Locate and identify every blood parasite.
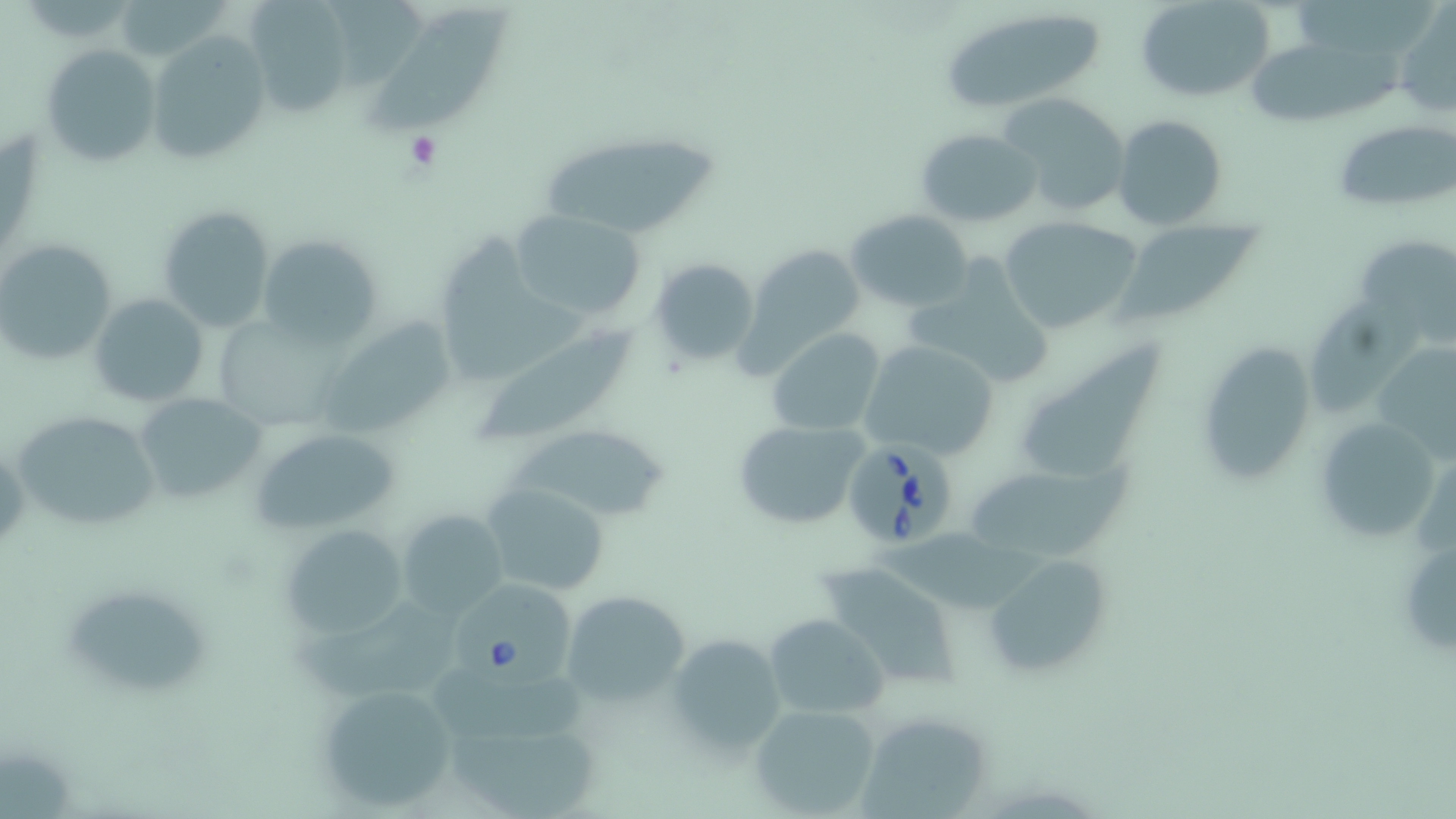
Approximate bounding boxes as (x1,y1)-(x2,y2) corner pairs in pixels.
Babesia divergens-infected red blood cells: (842,431)-(958,548), (448,585)-(576,690).
No Plasmodium falciparum, Plasmodium ovale, Plasmodium malariae, Plasmodium vivax, or Trypanosoma brucei observed.

slide-level diagnosis = Babesia divergens
image size = 1456×819 pixels
modality = light microscopy
stain = May-Grünwald-Giemsa
preparation = thin blood film
field of view = single
platelet locations = approximate bounding boxes as (x1,y1)-(x2,y2) corner pairs in pixels: (405,132)-(441,169)
uninfected red blood cell locations = approximate bounding boxes as (x1,y1)-(x2,y2) corner pairs in pixels: (330,0)-(428,87), (1134,0)-(1277,103), (121,1)-(228,58), (247,3)-(354,118), (937,4)-(1113,114), (369,6)-(512,134), (1393,10)-(1455,119), (147,33)-(267,162), (1248,40)-(1402,127), (40,45)-(159,168), (997,92)-(1131,217), (1113,114)-(1227,232), (1333,118)-(1456,213), (914,127)-(1041,228), (536,131)-(717,238), (157,208)-(274,331), (509,209)-(645,323), (845,209)-(974,312), (998,215)-(1143,336), (1120,215)-(1256,326), (1352,233)-(1456,335), (255,234)-(380,349), (0,238)-(116,365), (432,240)-(591,386), (745,245)-(865,362), (910,246)-(1051,394), (649,257)-(761,367), (88,293)-(209,407), (1314,298)-(1426,416), (319,319)-(455,438), (471,322)-(643,444), (767,328)-(885,437), (1024,331)-(1166,475), (859,337)-(1000,459), (1195,341)-(1320,489), (1373,341)-(1455,460), (134,394)-(263,506), (15,410)-(161,531), (1311,410)-(1444,548), (732,417)-(871,532), (509,420)-(673,525), (251,427)-(402,534), (971,466)-(1120,563), (479,483)-(611,598), (395,508)-(509,623), (278,523)-(412,638), (877,529)-(1040,609), (981,555)-(1110,679), (830,565)-(962,686), (559,589)-(692,707), (59,593)-(210,691), (287,606)-(464,696), (765,614)-(888,722), (666,633)-(786,757), (430,665)-(587,745), (314,682)-(461,813), (751,704)-(880,817), (860,712)-(994,819), (448,722)-(605,816), (0,744)-(76,819)
magnification = 1000x